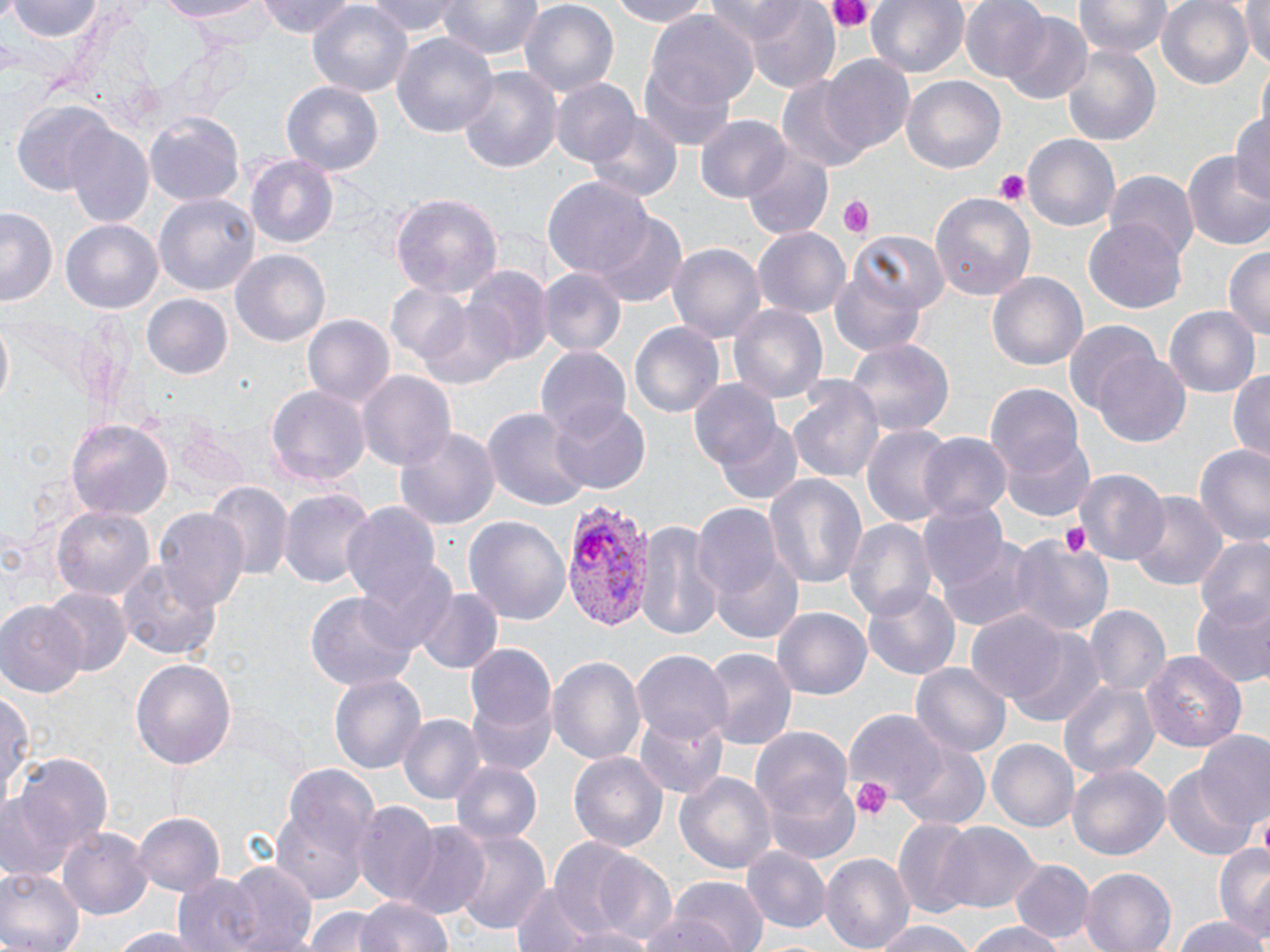
slide-level diagnosis = Plasmodium vivax
preparation = thin blood film
field of view = single
magnification = 1000x
modality = optical microscopy
uninfected red blood cell locations = approximate bounding boxes as (x1, y1, x2, y2) in pixels: (7, 0, 103, 44), (152, 0, 273, 24), (258, 0, 359, 39), (365, 0, 466, 39), (440, 0, 541, 62), (602, 0, 716, 27), (866, 0, 968, 80), (960, 0, 1053, 82), (1077, 0, 1173, 59), (1157, 0, 1253, 89), (1237, 0, 1268, 71), (308, 1, 412, 98), (516, 1, 621, 101), (720, 1, 843, 90), (995, 12, 1095, 106), (650, 13, 757, 113), (391, 29, 501, 141), (1057, 39, 1164, 150), (819, 56, 916, 157), (638, 61, 738, 150), (457, 65, 562, 177), (776, 74, 870, 172), (900, 76, 1005, 174), (549, 79, 641, 169), (281, 81, 383, 175), (12, 102, 116, 197), (586, 109, 682, 205), (1229, 111, 1270, 202), (145, 113, 245, 205), (697, 114, 790, 202), (62, 124, 153, 225), (1022, 133, 1120, 235), (744, 148, 833, 239), (1184, 149, 1270, 254), (245, 155, 340, 251), (1103, 171, 1199, 261), (543, 176, 653, 282), (929, 192, 1037, 299), (155, 193, 258, 296), (390, 193, 503, 301), (1, 206, 59, 305), (595, 215, 687, 306), (1086, 218, 1187, 315), (62, 222, 162, 311), (753, 227, 850, 318), (850, 229, 950, 316), (669, 240, 766, 344), (1225, 247, 1270, 345), (229, 249, 331, 350), (461, 266, 551, 366), (536, 267, 626, 356), (829, 267, 928, 357), (989, 272, 1088, 373), (386, 283, 472, 367), (143, 295, 232, 378), (729, 303, 829, 406), (1162, 305, 1259, 397), (303, 315, 395, 410), (1063, 318, 1169, 426), (630, 321, 724, 419), (845, 336, 954, 441), (535, 345, 631, 436), (1090, 354, 1191, 445), (1227, 368, 1270, 462), (357, 371, 456, 474), (785, 378, 886, 484), (688, 380, 785, 474), (266, 384, 371, 486), (988, 385, 1086, 482), (549, 402, 650, 493), (481, 405, 594, 511), (67, 419, 174, 519), (712, 419, 805, 506), (177, 424, 249, 493), (395, 424, 500, 529), (863, 425, 952, 527), (918, 432, 1012, 522), (1001, 434, 1097, 522), (1194, 441, 1270, 549), (1076, 469, 1170, 567), (765, 472, 869, 589), (204, 483, 290, 584), (277, 488, 373, 588), (1130, 491, 1225, 592), (916, 502, 1009, 597), (341, 503, 443, 610), (691, 505, 783, 601), (52, 506, 152, 601), (153, 508, 251, 613), (464, 515, 570, 626), (844, 517, 934, 623), (639, 521, 722, 643), (930, 532, 1037, 630), (1194, 536, 1270, 634), (1008, 538, 1112, 638), (709, 553, 804, 646), (117, 560, 220, 662), (350, 561, 459, 657), (863, 583, 959, 681), (414, 587, 502, 675), (43, 588, 131, 676), (304, 591, 421, 691), (1190, 597, 1270, 688), (0, 602, 85, 697), (1083, 605, 1168, 700), (771, 608, 871, 700), (966, 611, 1069, 707), (1009, 629, 1105, 727), (465, 642, 557, 736), (702, 646, 796, 749), (634, 651, 733, 744), (1141, 651, 1247, 751), (549, 654, 645, 770), (131, 659, 237, 769), (912, 663, 1010, 762), (328, 673, 427, 777), (1056, 680, 1157, 780), (1, 688, 35, 814), (466, 694, 558, 776), (639, 708, 729, 799), (845, 710, 947, 804), (397, 714, 483, 805), (752, 727, 852, 818), (1196, 736, 1270, 834), (989, 739, 1078, 833), (896, 742, 990, 831), (569, 751, 669, 855), (3, 755, 114, 883), (452, 761, 543, 848), (1067, 763, 1169, 860), (1162, 767, 1255, 859), (675, 770, 776, 877), (271, 772, 376, 900), (763, 778, 862, 866), (357, 803, 439, 901), (133, 812, 227, 897), (894, 818, 982, 918), (396, 823, 489, 917), (939, 823, 1040, 915), (59, 825, 154, 919), (452, 828, 549, 937), (562, 844, 676, 943), (1214, 845, 1269, 944), (740, 847, 830, 934), (820, 852, 913, 952), (1011, 859, 1094, 946), (224, 862, 318, 951), (0, 867, 84, 952), (1081, 868, 1179, 952), (171, 874, 265, 952), (669, 877, 769, 952), (511, 880, 598, 952), (354, 894, 455, 952), (634, 905, 749, 952), (304, 907, 383, 952), (1171, 914, 1269, 952), (872, 920, 977, 952), (966, 920, 1062, 952), (563, 926, 658, 952), (102, 927, 221, 951)
stain = May-Grünwald-Giemsa
platelet locations = approximate bounding boxes as (x1, y1, x2, y2) in pixels: (824, 0, 874, 34), (993, 169, 1031, 204), (838, 195, 875, 239), (1061, 519, 1091, 558), (851, 778, 892, 820)
image size = 1270×952 pixels
Plasmodium vivax-infected red blood cell locations = approximate bounding boxes as (x1, y1, x2, y2) in pixels: (559, 497, 658, 631)